Identify the parasite.
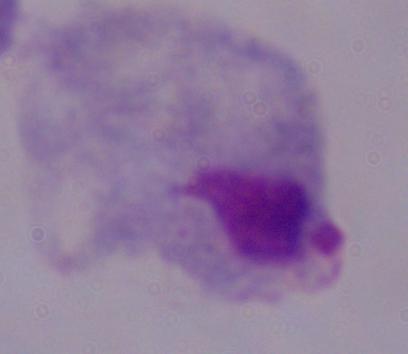
A trichomonad.

Summary:
  - Magnification: 1000x
  - Modality: photomicrograph